Locate and identify every blood parasite.
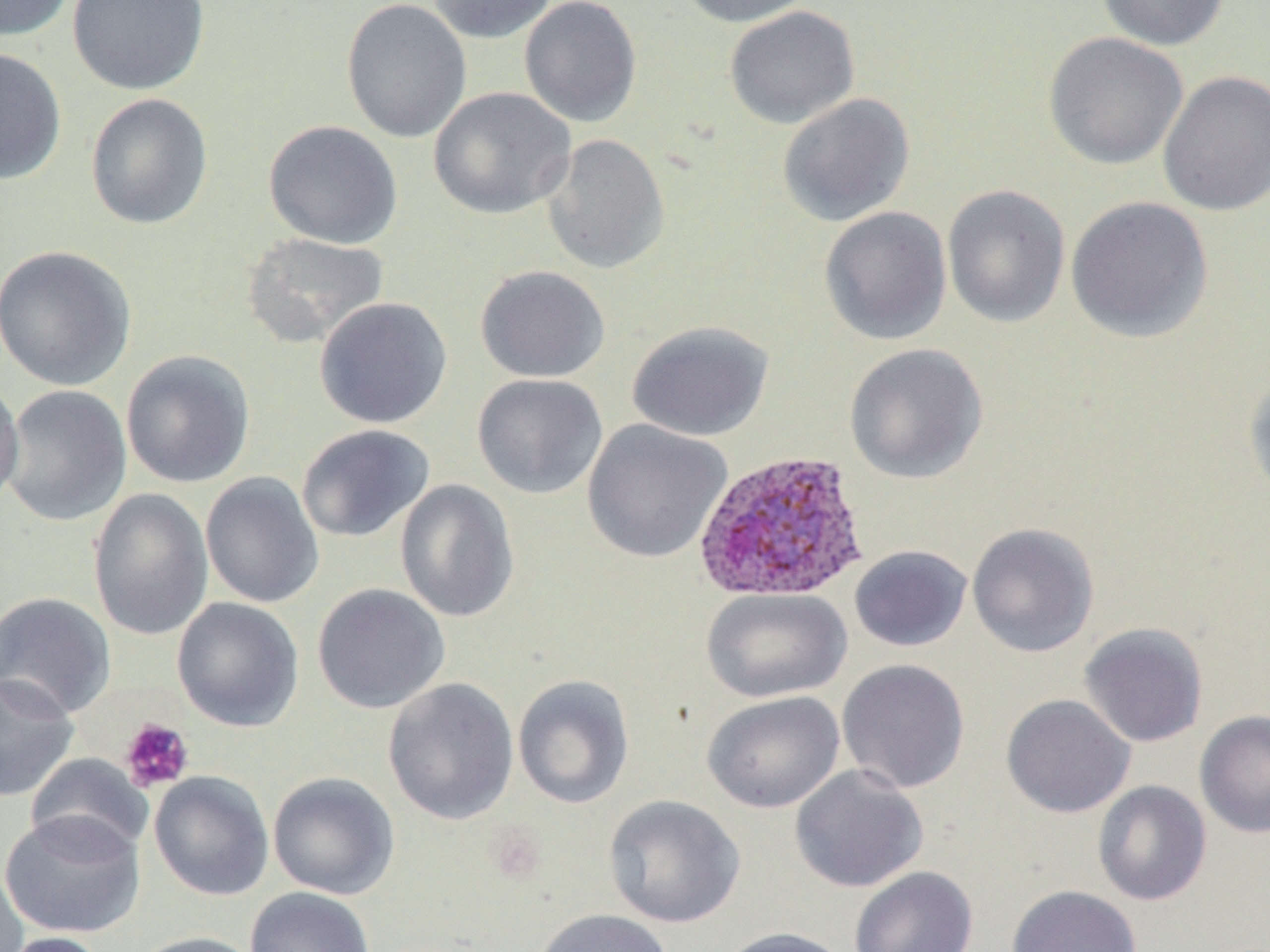
Approximate bounding boxes as (x1,y1)-(x2,y2) corner pairs in pixels.
Plasmodium ovale-infected red blood cells: (693,449)-(870,604).
No Plasmodium falciparum, Plasmodium malariae, Plasmodium vivax, Babesia divergens, or Trypanosoma brucei observed.

Platelet locations: (119,718)-(194,793). Uninfected red blood cell locations: (0,0)-(75,41), (68,0)-(210,95), (341,0)-(472,143), (427,0)-(559,44), (519,0)-(642,127), (674,0)-(820,27), (1096,0)-(1231,51), (723,5)-(860,129), (1043,32)-(1189,170), (0,47)-(67,185), (1157,70)-(1270,217), (428,86)-(576,220), (84,92)-(214,230), (777,93)-(915,226), (263,120)-(403,249), (541,134)-(671,275), (941,184)-(1070,329), (1065,196)-(1213,343), (819,206)-(952,345), (240,232)-(390,349), (0,244)-(138,391), (475,265)-(610,383), (313,296)-(453,428), (627,319)-(774,441), (843,343)-(989,484), (121,349)-(255,488), (1242,372)-(1270,506), (472,373)-(608,499), (0,374)-(24,514), (1,385)-(132,527), (582,419)-(732,564), (296,424)-(435,542), (200,472)-(324,608), (395,479)-(520,623), (87,488)-(213,641), (966,522)-(1100,658), (849,545)-(972,652), (312,583)-(450,714), (701,587)-(851,703), (0,591)-(116,720), (171,597)-(304,732), (1078,622)-(1209,748), (836,658)-(971,794), (0,672)-(79,802), (513,674)-(634,809), (383,677)-(519,825), (702,690)-(844,814), (1001,694)-(1135,818), (1194,709)-(1270,839), (25,753)-(153,859), (790,764)-(928,893), (149,771)-(274,901), (268,771)-(400,900), (1092,780)-(1212,906), (603,794)-(745,928), (0,810)-(145,938), (0,861)-(29,952), (849,866)-(979,952), (1006,885)-(1142,952), (245,887)-(376,952), (530,908)-(673,952), (715,926)-(853,952), (1,931)-(107,952), (126,931)-(266,952). Slide-level diagnosis: Plasmodium ovale. Image is 1270×952 pixels. Single field of view. Thin blood smear. Optical microscopy. May-Grünwald-Giemsa stain. Captured at 1000x magnification.